Classify this cell by malaria status.
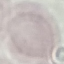
It is uninfected.

Summary:
  - Preparation: thin blood smear
  - Image type: automatically extracted cell patch, resized to 64 × 64 pixels
  - Stain: Giemsa
  - Capture: smartphone camera at the microscope eyepiece